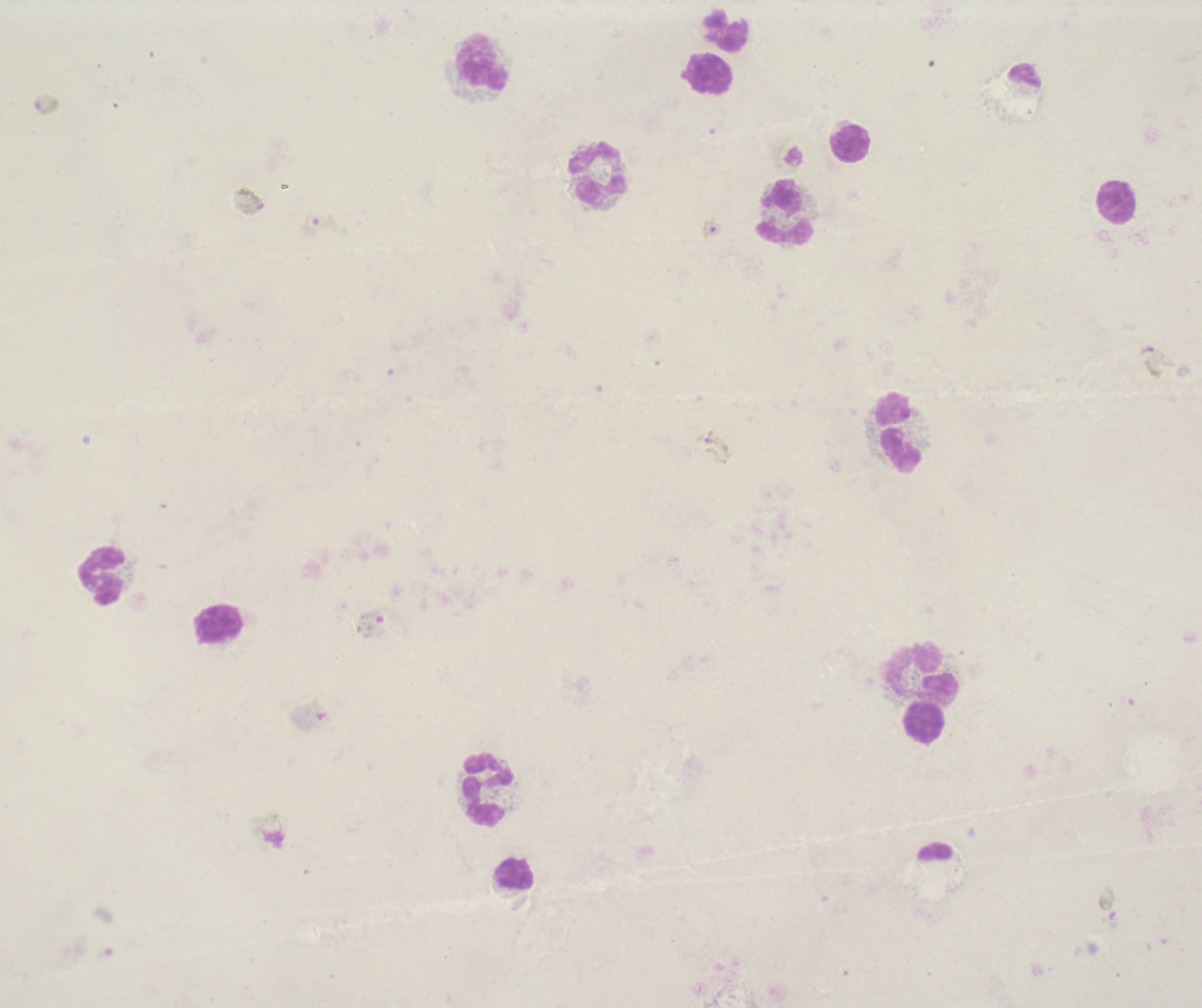

coordinate format = approximate centers as [x, y] in pixels
leukocyte locations = [727, 31], [484, 62], [709, 74], [850, 144], [599, 173], [1116, 201], [786, 212], [899, 433], [103, 576], [218, 625], [922, 675], [925, 723], [487, 789], [515, 875]
gametocyte locations = [46, 105], [790, 155], [250, 201], [711, 229], [1153, 362], [714, 447], [373, 625], [311, 717], [269, 830], [1107, 906]
field of view = one from this slide
stain = Romanowsky
image size = 1202×1008 pixels
context = previously used in an actual diagnosis
coloration quality = bad
result = Plasmodium parasites identified
preparation = thick blood smear
magnification = 100x
background quality = unsatisfactory